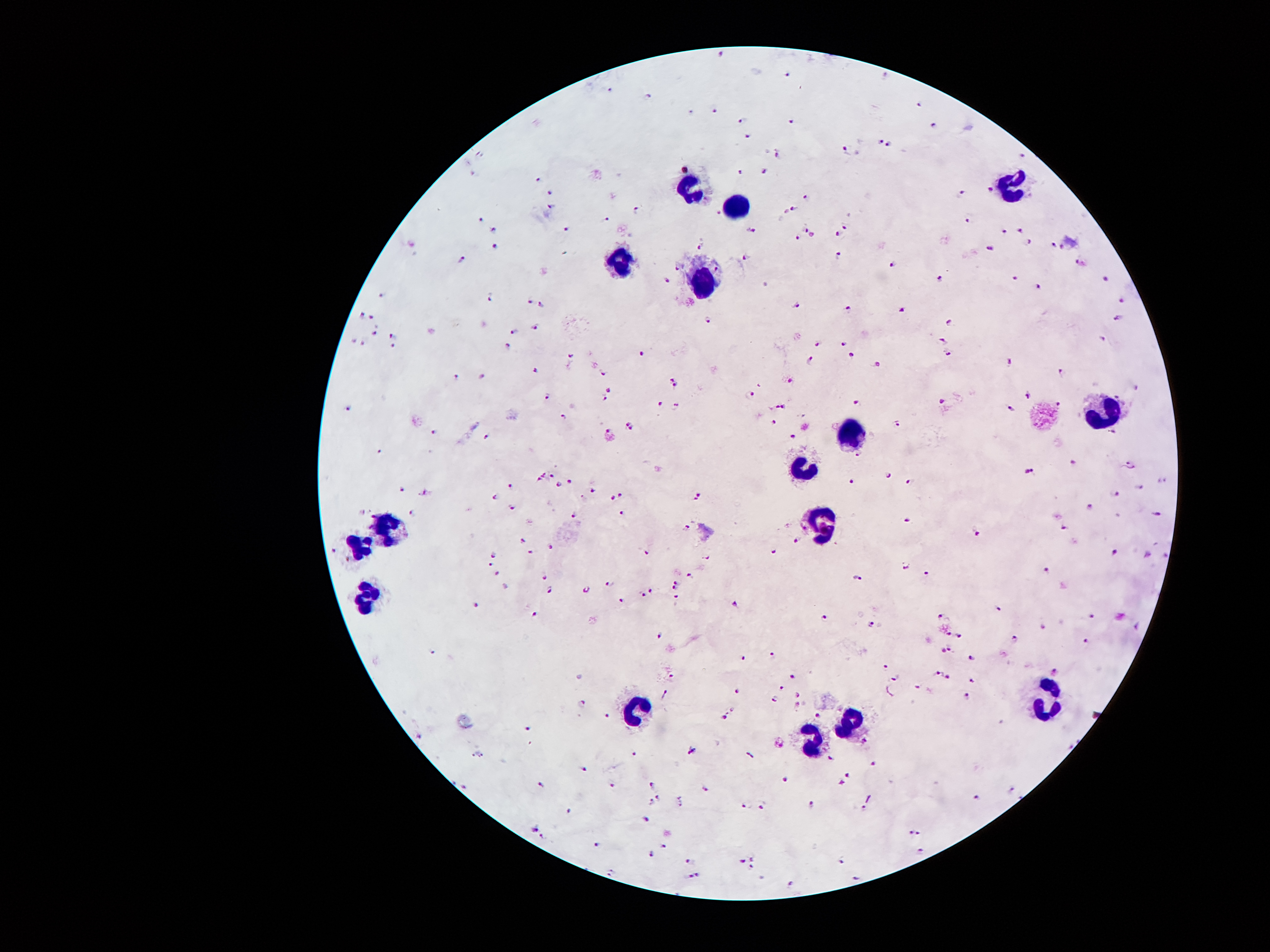

{
  "leukocyte_locations": "approximate centers as (x, y) in pixels: (1009, 182), (687, 186), (735, 207), (623, 263), (701, 277), (1107, 411), (855, 434), (805, 472), (825, 527), (389, 531), (357, 544), (367, 597), (1046, 699), (637, 708), (848, 722), (805, 743)",
  "plasmodium_parasite_locations": "approximate centers as (x, y) in pixels: (721, 56), (786, 75), (608, 90), (648, 97), (918, 104), (714, 111), (742, 120), (791, 122), (935, 126), (750, 138), (879, 143), (889, 146), (845, 151), (777, 154), (1021, 156), (766, 171), (741, 172), (538, 181), (989, 188), (961, 192), (550, 195), (805, 197), (550, 207), (794, 209), (636, 212), (787, 212), (967, 219), (481, 220), (606, 221), (845, 227), (806, 228), (493, 230), (564, 231), (750, 231), (1020, 231), (836, 233), (1005, 233), (812, 236), (797, 237), (1030, 243), (1053, 245), (494, 247), (699, 247), (991, 249), (838, 255), (746, 257), (461, 261), (1080, 264), (893, 265), (675, 266), (939, 278), (1014, 278), (1105, 278), (668, 280), (1039, 286), (383, 294), (492, 297), (1122, 300), (529, 301), (541, 305), (798, 305), (849, 308), (900, 309), (360, 315), (372, 318), (1117, 318), (708, 320), (951, 322), (535, 326), (375, 332), (515, 332), (392, 336), (352, 340), (940, 340), (843, 342), (819, 343), (362, 344), (392, 346), (508, 346), (570, 353), (641, 354), (948, 354), (851, 355), (811, 360), (1008, 361), (878, 363), (535, 371), (1063, 371), (603, 374), (481, 376), (456, 378), (671, 378), (788, 380), (675, 384), (610, 390), (751, 394), (1028, 394), (544, 398), (605, 401), (941, 401), (658, 404), (858, 404), (1058, 404), (672, 406), (348, 407), (785, 407), (773, 408), (1011, 409), (775, 422), (897, 423), (435, 432), (1113, 433), (486, 436), (793, 436), (379, 453), (858, 455), (1072, 462), (1129, 464), (1029, 471), (888, 474), (552, 476), (540, 479), (908, 480), (567, 481), (852, 481), (558, 485), (509, 487), (1139, 487), (400, 490), (590, 490), (423, 493), (620, 494), (698, 495), (1115, 495), (494, 497), (613, 498), (1089, 505), (511, 506), (412, 513), (622, 513), (1156, 513), (574, 516), (905, 521), (686, 526), (1064, 529), (977, 533), (795, 539), (523, 540), (552, 547), (331, 551), (529, 552), (1113, 552), (646, 553), (772, 553), (494, 555), (707, 555), (1146, 555), (1165, 557), (490, 563), (906, 564), (925, 571), (497, 573), (1046, 573), (690, 576), (857, 576), (543, 578), (675, 582), (610, 584), (550, 589), (673, 589), (649, 590), (584, 591), (641, 594), (674, 597), (619, 601), (476, 603), (735, 605), (996, 609), (941, 614), (534, 615), (827, 617), (1090, 617), (873, 623), (1137, 627), (947, 633), (660, 636), (960, 637), (1014, 639), (1086, 644), (950, 649), (940, 650), (772, 655), (744, 657), (971, 657), (887, 666), (1056, 670), (937, 673), (671, 675), (791, 676), (946, 676), (895, 677), (971, 679), (917, 685), (781, 688), (736, 693), (797, 695), (665, 696), (964, 697), (774, 701), (581, 706), (816, 714), (607, 715), (722, 719), (527, 729), (863, 739), (690, 753), (748, 754), (632, 755), (830, 757), (874, 764), (582, 766), (847, 775), (785, 781), (540, 782), (651, 784), (840, 784), (612, 786), (703, 788), (1011, 789), (975, 796), (658, 798), (678, 800), (650, 803), (810, 805), (745, 806), (762, 807), (865, 811), (569, 812), (644, 815), (534, 830), (909, 833), (919, 835), (542, 836), (594, 844), (662, 846), (923, 851), (649, 853), (753, 858), (690, 862), (741, 862), (840, 864), (753, 867), (613, 873), (699, 875), (689, 877), (854, 877), (790, 884)",
  "magnification": "100x",
  "stain": "Giemsa",
  "field_of_view": "one from this slide",
  "preparation": "thick blood smear",
  "capture": "smartphone through the microscope eyepiece",
  "image_size": "1270×952 pixels",
  "patient_malaria_status": "positive for Plasmodium falciparum"
}